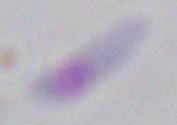

Summary:
  - Modality: micrograph
  - Magnification: 1000x
  - Identification: Toxoplasma gondii